Outline each Plasmodium falciparum-infected red blood cell.
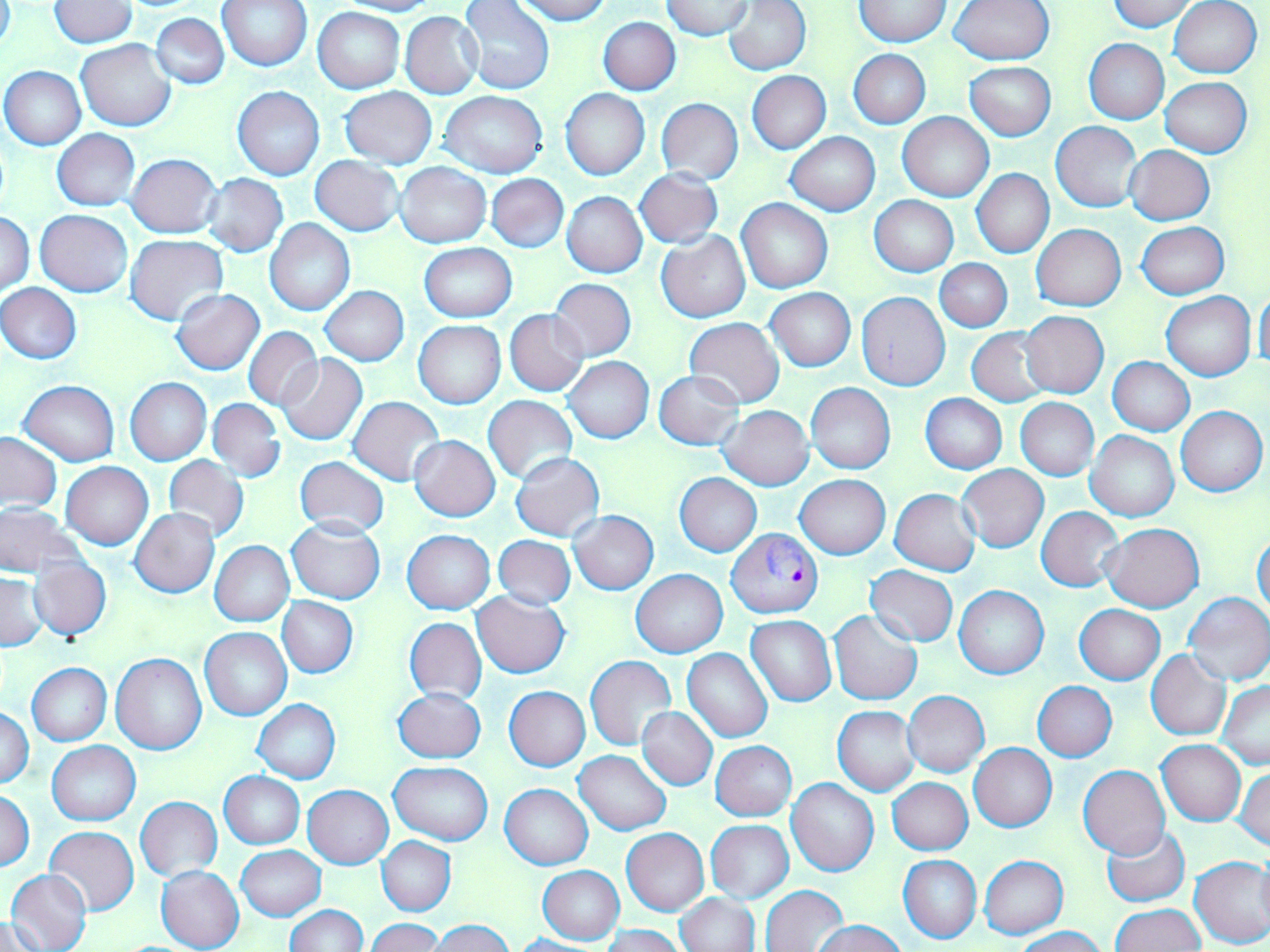
Approximate bounding boxes as (x1,y1)-(x2,y2) corner pairs in pixels.
Plasmodium falciparum-infected red blood cells: (726,528)-(824,617).

Summary:
  - Uninfected red blood cell locations: (217,0)-(312,71), (336,0)-(439,15), (513,0)-(611,24), (660,0)-(755,40), (724,0)-(811,74), (950,0)-(1054,66), (1109,0)-(1198,31), (1169,0)-(1262,78), (459,1)-(556,96), (854,1)-(951,47), (48,2)-(136,49), (314,7)-(405,93), (401,12)-(484,99), (151,13)-(229,89), (599,17)-(680,94), (1084,39)-(1169,124), (76,40)-(176,130), (848,49)-(931,129), (966,62)-(1056,140), (1,66)-(86,150), (747,71)-(830,153), (1160,78)-(1252,158), (232,86)-(325,180), (339,86)-(437,167), (561,88)-(650,180), (440,91)-(549,178), (656,98)-(743,184), (898,112)-(994,201), (1051,121)-(1144,213), (52,129)-(139,211), (785,132)-(879,215), (1125,146)-(1215,225), (126,153)-(222,238), (310,156)-(405,235), (395,163)-(491,248), (635,168)-(724,249), (972,169)-(1053,258), (201,173)-(288,257), (486,173)-(568,253), (562,192)-(647,277), (870,195)-(958,276), (736,198)-(833,293), (35,210)-(132,297), (1,211)-(35,295), (265,218)-(355,315), (1137,221)-(1229,299), (1032,224)-(1125,311), (657,231)-(749,322), (126,234)-(229,325), (419,242)-(516,320), (935,259)-(1012,333), (549,279)-(636,361), (1,283)-(82,364), (319,285)-(409,365), (1255,286)-(1270,374), (171,288)-(266,375), (765,288)-(856,371), (855,292)-(951,390), (1162,292)-(1255,381), (504,309)-(589,396), (1018,311)-(1108,398), (684,317)-(784,408), (414,320)-(506,408), (244,327)-(323,411), (967,328)-(1054,406), (276,354)-(367,446), (564,357)-(654,444), (1107,357)-(1194,435), (655,370)-(745,451), (125,377)-(211,465), (19,380)-(119,466), (806,383)-(895,474), (921,394)-(1007,473), (483,396)-(578,483), (347,397)-(444,484), (1015,398)-(1098,480), (207,399)-(285,482), (719,405)-(813,490), (1176,405)-(1267,497), (1086,430)-(1178,522), (0,432)-(62,510), (409,435)-(500,520), (511,452)-(604,542), (164,455)-(249,543), (295,455)-(390,539), (61,463)-(153,549), (958,465)-(1048,551), (674,473)-(762,556), (796,475)-(889,560), (890,489)-(980,576), (0,504)-(82,576), (1037,506)-(1124,592), (131,509)-(219,598), (569,512)-(659,594), (286,517)-(386,604), (1101,523)-(1205,611), (402,530)-(495,613), (1252,533)-(1270,620), (493,535)-(576,609), (210,541)-(294,627), (29,559)-(111,641), (864,564)-(958,647), (631,569)-(727,658), (0,572)-(47,651), (954,585)-(1049,679), (1184,591)-(1270,686), (472,592)-(570,677), (277,597)-(358,678), (1074,604)-(1165,684), (829,610)-(923,705), (746,616)-(836,706), (406,617)-(486,704), (200,627)-(291,720), (682,648)-(772,742), (1147,651)-(1232,740), (111,653)-(206,754), (585,655)-(677,751), (26,662)-(112,746), (1033,681)-(1117,761), (1219,681)-(1270,768), (504,685)-(590,771), (392,687)-(486,764), (902,691)-(989,776), (252,699)-(341,784), (834,706)-(920,795), (0,707)-(34,789), (637,707)-(717,790), (1157,740)-(1246,826), (46,741)-(141,825), (711,741)-(796,821), (969,743)-(1056,832), (574,750)-(672,834), (388,761)-(493,845), (1079,765)-(1170,858), (1233,767)-(1270,850), (219,772)-(305,849), (888,778)-(972,855), (786,779)-(879,878), (499,784)-(592,869), (303,785)-(394,868), (2,789)-(35,872), (135,797)-(222,881), (706,820)-(793,902), (44,826)-(139,915), (1101,826)-(1189,907), (621,828)-(709,915), (378,837)-(455,916), (236,845)-(325,921), (1257,850)-(1270,929), (979,854)-(1068,938), (899,855)-(981,943), (1189,855)-(1270,949), (156,865)-(244,952), (538,866)-(624,945), (7,868)-(92,952), (761,885)-(849,952), (677,893)-(760,952), (1108,904)-(1205,952), (284,905)-(366,952), (3,915)-(44,951), (366,918)-(443,951), (431,920)-(514,952), (814,920)-(905,952), (603,924)-(685,952), (1013,927)-(1106,952), (510,934)-(605,952)
  - Slide-level diagnosis: Plasmodium falciparum
  - Field of view: one of a larger specimen
  - Image size: 1270×952 pixels
  - Modality: optical microscopy
  - Preparation: thin blood smear
  - Stain: May-Grünwald-Giemsa
  - Magnification: 1000x